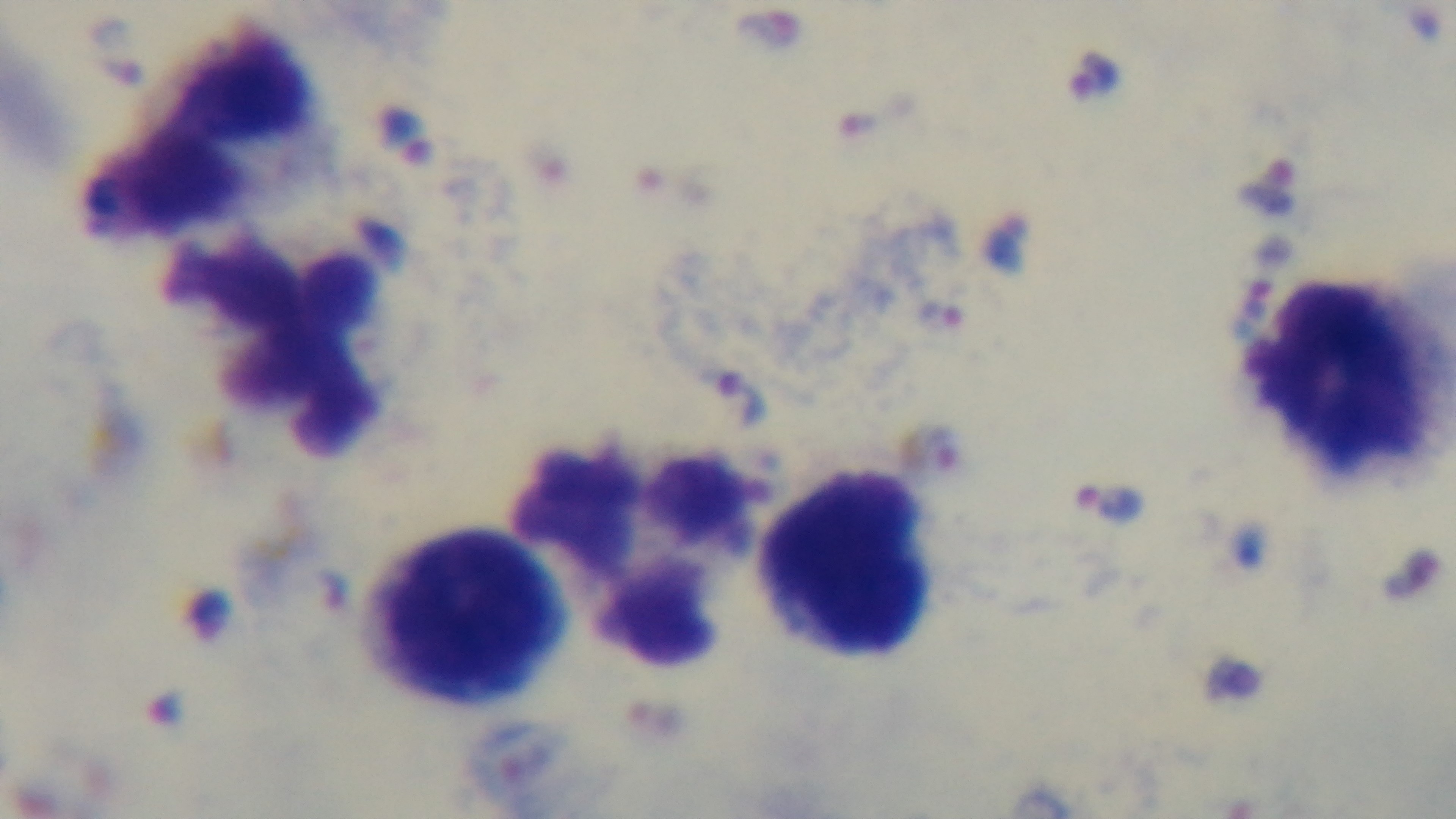
Summary:
  - Modality: light microscopy
  - Preparation: thick smear
  - Stain: Giemsa
  - Field of view: single
  - Capture: mounted 4K digital camera
  - Objective: 100x oil immersion
  - Malaria status: positive